State the preparation type.
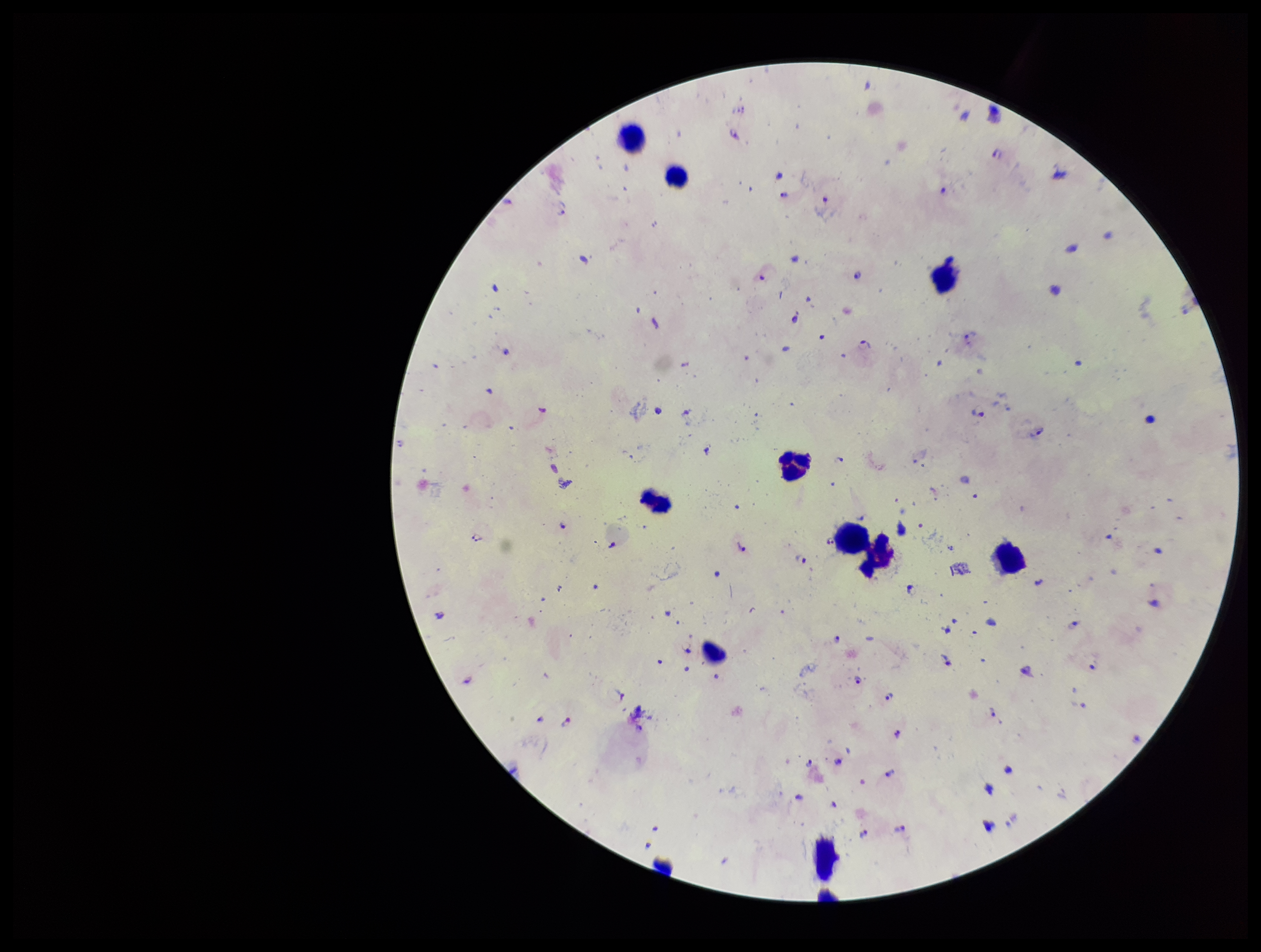

A thick smear.

capture = smartphone photograph through the microscope eyepiece
field of view = one from this slide
Plasmodium parasites = detected
leukocyte count = 40
image size = 1261×952 pixels
stain = Giemsa
parasite count = 39
species reported for this patient = Plasmodium falciparum
patient malaria status = infected